Assess this cell for malaria.
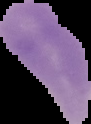
Uninfected.

Summary:
  - Preparation: thin blood film
  - Image type: cell region segmented out of the field of view; surrounding area masked to black
  - Image size: 91×124 pixels